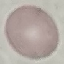

malaria status = uninfected
image type = cell patch, automatically extracted from a larger field of view and resized to 64 × 64 pixels
capture = smartphone through the microscope eyepiece
preparation = thin blood film
stain = Giemsa